Classify this cell by malaria status.
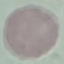
It is uninfected.

Acquired by smartphone through the microscope eyepiece. Thin smear of blood. Cell patch, automatically extracted from a larger field of view and resized to 64 × 64 pixels. Giemsa stain.